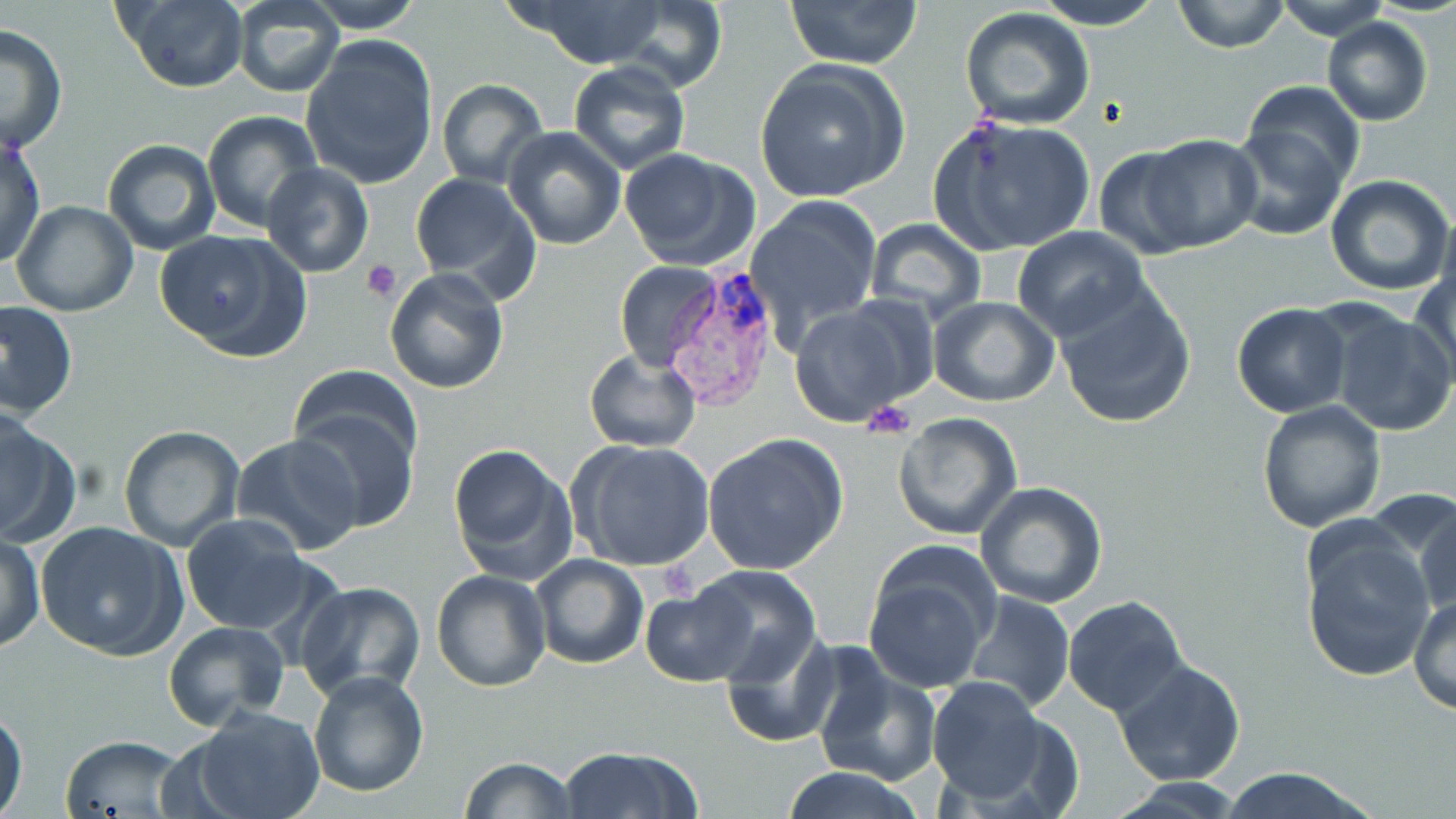

Summary:
  - Coordinate format: approximate bounding boxes as [x1, y1, x2, y2] in pixels
  - Uninfected red blood cell locations: [113, 0, 249, 92], [231, 0, 344, 98], [521, 0, 674, 68], [786, 0, 923, 69], [1029, 0, 1169, 30], [1173, 0, 1289, 54], [1275, 0, 1391, 41], [304, 1, 424, 32], [605, 1, 729, 91], [958, 8, 1097, 131], [1322, 16, 1432, 126], [0, 25, 67, 156], [301, 35, 439, 190], [567, 60, 690, 174], [754, 60, 910, 203], [437, 78, 548, 187], [1243, 82, 1365, 191], [203, 111, 324, 230], [929, 116, 1097, 255], [1226, 123, 1349, 242], [501, 128, 627, 250], [1, 132, 46, 267], [1140, 136, 1260, 250], [102, 139, 221, 256], [1092, 148, 1200, 255], [619, 149, 761, 272], [262, 162, 373, 277], [409, 173, 543, 302], [1325, 175, 1456, 296], [746, 196, 884, 338], [11, 199, 139, 317], [864, 220, 987, 327], [1011, 226, 1150, 343], [154, 229, 310, 362], [614, 260, 721, 371], [1410, 266, 1456, 388], [385, 269, 509, 393], [1054, 283, 1197, 429], [929, 297, 1059, 405], [0, 299, 77, 420], [789, 300, 929, 426], [1231, 303, 1353, 418], [1323, 305, 1456, 437], [583, 347, 703, 454], [289, 361, 423, 470], [1256, 401, 1386, 535], [288, 403, 420, 531], [0, 411, 79, 550], [892, 411, 1023, 539], [117, 425, 245, 552], [703, 434, 849, 575], [234, 435, 364, 556], [570, 439, 717, 573], [447, 440, 577, 585], [94, 453, 242, 618], [976, 480, 1109, 607], [1365, 485, 1456, 605], [1411, 493, 1455, 619], [181, 513, 315, 635], [33, 522, 187, 659], [1300, 526, 1436, 682], [1, 535, 46, 652], [863, 553, 996, 694], [530, 555, 649, 671], [687, 565, 822, 684], [431, 569, 551, 692], [295, 580, 427, 703], [638, 583, 754, 689], [960, 590, 1075, 714], [1411, 594, 1456, 715], [1062, 596, 1188, 718], [162, 620, 291, 730], [722, 629, 841, 747], [813, 658, 941, 786], [1114, 660, 1245, 787], [309, 668, 430, 796], [927, 677, 1050, 804], [0, 700, 27, 818], [186, 707, 326, 819], [58, 733, 188, 817], [556, 745, 702, 819], [459, 757, 580, 818], [782, 766, 920, 819], [1214, 767, 1381, 819], [1105, 779, 1251, 817]
  - Plasmodium vivax-infected red blood cell locations: [655, 264, 787, 416]
  - Platelet locations: [362, 260, 404, 302], [859, 399, 916, 439], [655, 555, 700, 607]
  - Slide-level diagnosis: Plasmodium vivax
  - Stain: May-Grünwald-Giemsa
  - Modality: optical microscopy
  - Field of view: single
  - Image size: 1456×819 pixels
  - Preparation: thin blood smear
  - Magnification: 1000x